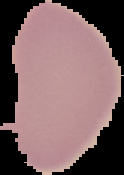

preparation = thin blood film
image type = segmented cell region on a black background
malaria status = uninfected
image size = 124×175 pixels